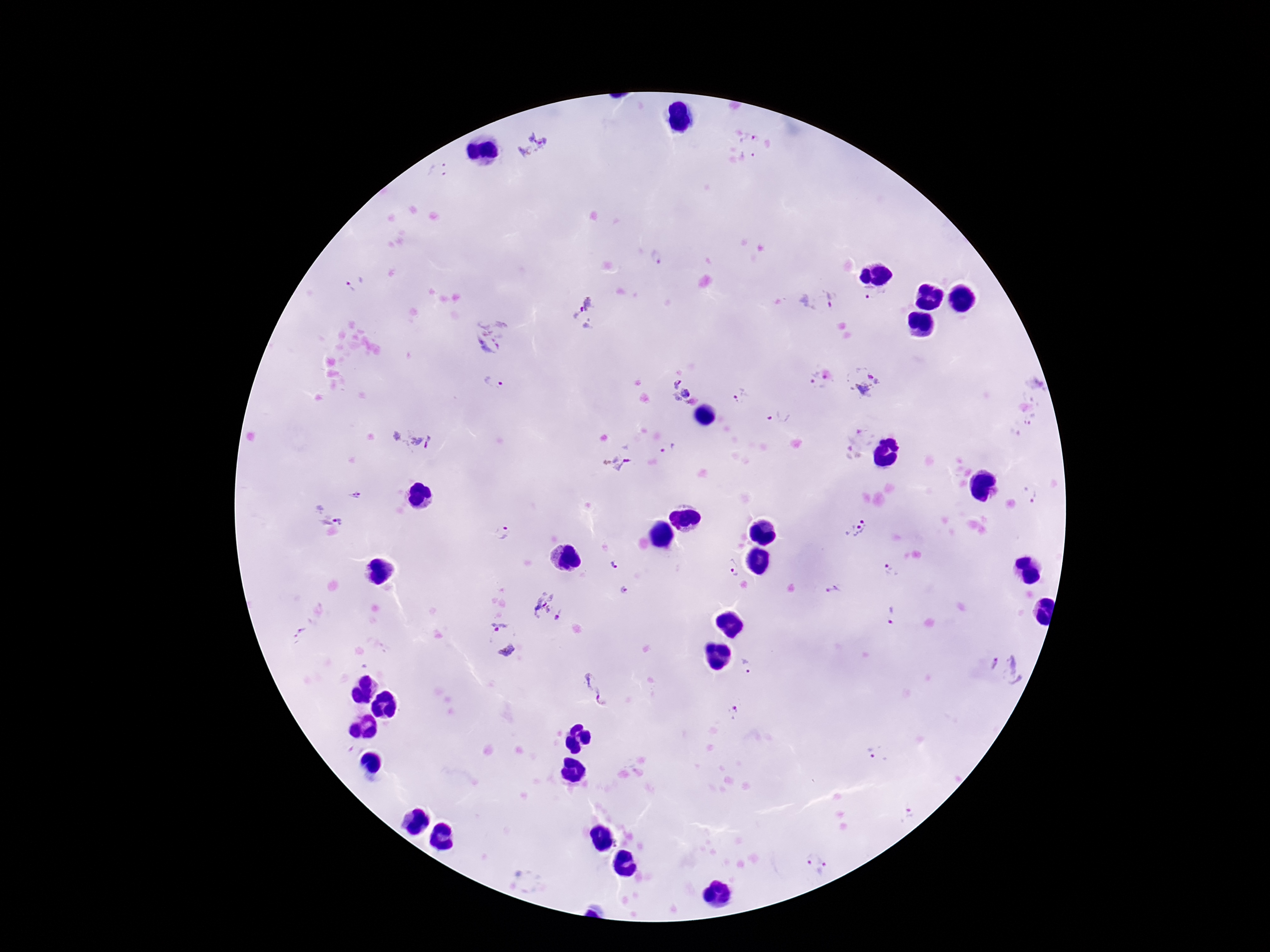

Plasmodium parasite locations = approximate centers as {x, y} in pixels: {533, 143}, {756, 145}, {438, 169}, {655, 257}, {354, 284}, {873, 295}, {815, 299}, {585, 315}, {492, 335}, {493, 382}, {815, 382}, {864, 383}, {1035, 383}, {679, 389}, {742, 398}, {781, 416}, {1025, 425}, {410, 439}, {854, 441}, {672, 452}, {617, 462}, {1030, 493}, {355, 495}, {332, 509}, {856, 528}, {503, 534}, {615, 564}, {732, 569}, {891, 570}, {834, 590}, {627, 591}, {547, 607}, {892, 614}, {300, 633}, {501, 639}, {747, 666}, {1006, 668}, {593, 688}, {733, 712}, {873, 754}, {908, 816}, {815, 865}
stain = Giemsa
field of view = single
preparation = thick peripheral-blood smear
patient malaria status = positive
capture = smartphone camera through the microscope eyepiece
magnification = 100x
image size = 1270×952 pixels